Give the position of every Plasmodium parasite and every leukocyte.
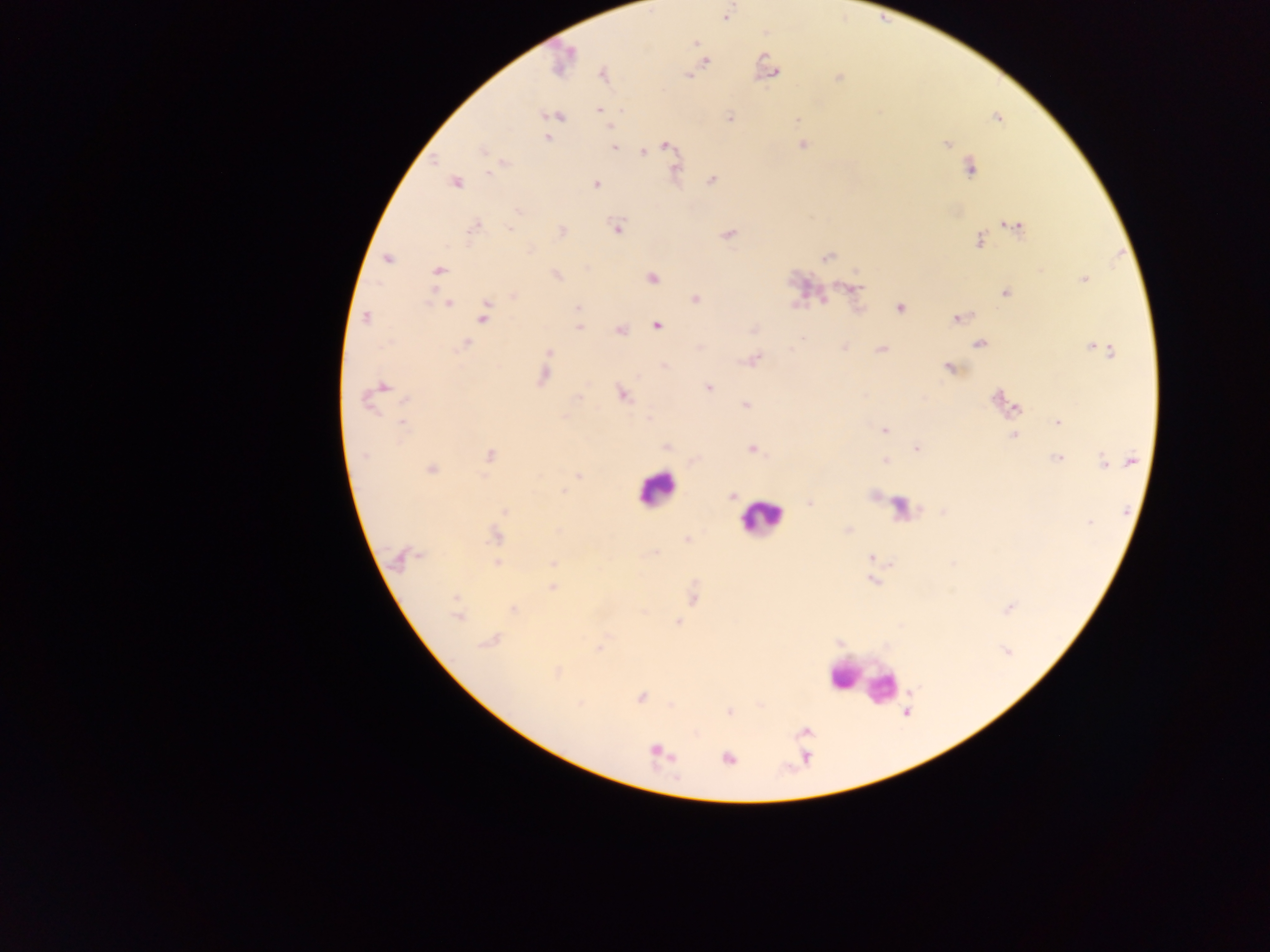
Approximate centers as [x, y] in pixels.
Plasmodium parasites: [726, 16], [695, 43], [562, 61], [705, 62], [769, 65], [773, 73], [603, 75], [838, 78], [599, 109], [557, 115], [729, 118], [797, 119], [547, 138], [947, 144], [803, 145], [667, 146], [614, 148], [482, 150], [643, 151], [675, 167], [970, 168], [489, 174], [712, 180], [456, 183], [596, 184], [519, 212], [474, 227], [617, 227], [1015, 227], [510, 228], [561, 231], [728, 234], [980, 240], [827, 257], [387, 258], [439, 270], [556, 275], [652, 278], [1082, 279], [855, 287], [1004, 293], [514, 295], [696, 299], [448, 304], [577, 308], [901, 308], [484, 315], [366, 318], [956, 318], [656, 325], [579, 328], [621, 331], [465, 344], [979, 344], [844, 348], [881, 349], [1101, 349], [550, 352], [753, 359], [665, 366], [950, 368], [544, 377], [383, 386], [709, 388], [623, 394], [577, 397], [407, 399], [997, 399], [367, 401], [1008, 403], [746, 405], [1015, 407], [650, 419], [403, 422], [1057, 422], [884, 430], [1014, 436], [666, 447], [917, 448], [752, 449], [364, 455], [489, 455], [1058, 458], [1113, 460], [885, 461], [1130, 461], [1103, 462], [431, 470], [578, 475], [565, 492], [732, 496], [811, 503], [504, 511], [848, 530], [496, 536], [686, 539], [654, 554], [870, 556], [418, 557], [398, 559], [496, 563], [552, 563], [872, 581], [552, 588], [455, 597], [512, 609], [1009, 609], [458, 617], [678, 621], [489, 641], [599, 649], [558, 672], [640, 698], [729, 712], [657, 752], [728, 758].
Leukocytes: [654, 490], [761, 519], [861, 683], [881, 689].

field of view = single
country = Ghana
image size = 1270×952 pixels
capture = mobile-phone photograph through a microscope
preparation = thick blood film